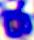

modality = micrograph
identification = white blood cell
magnification = 400x